Outline white blood cells.
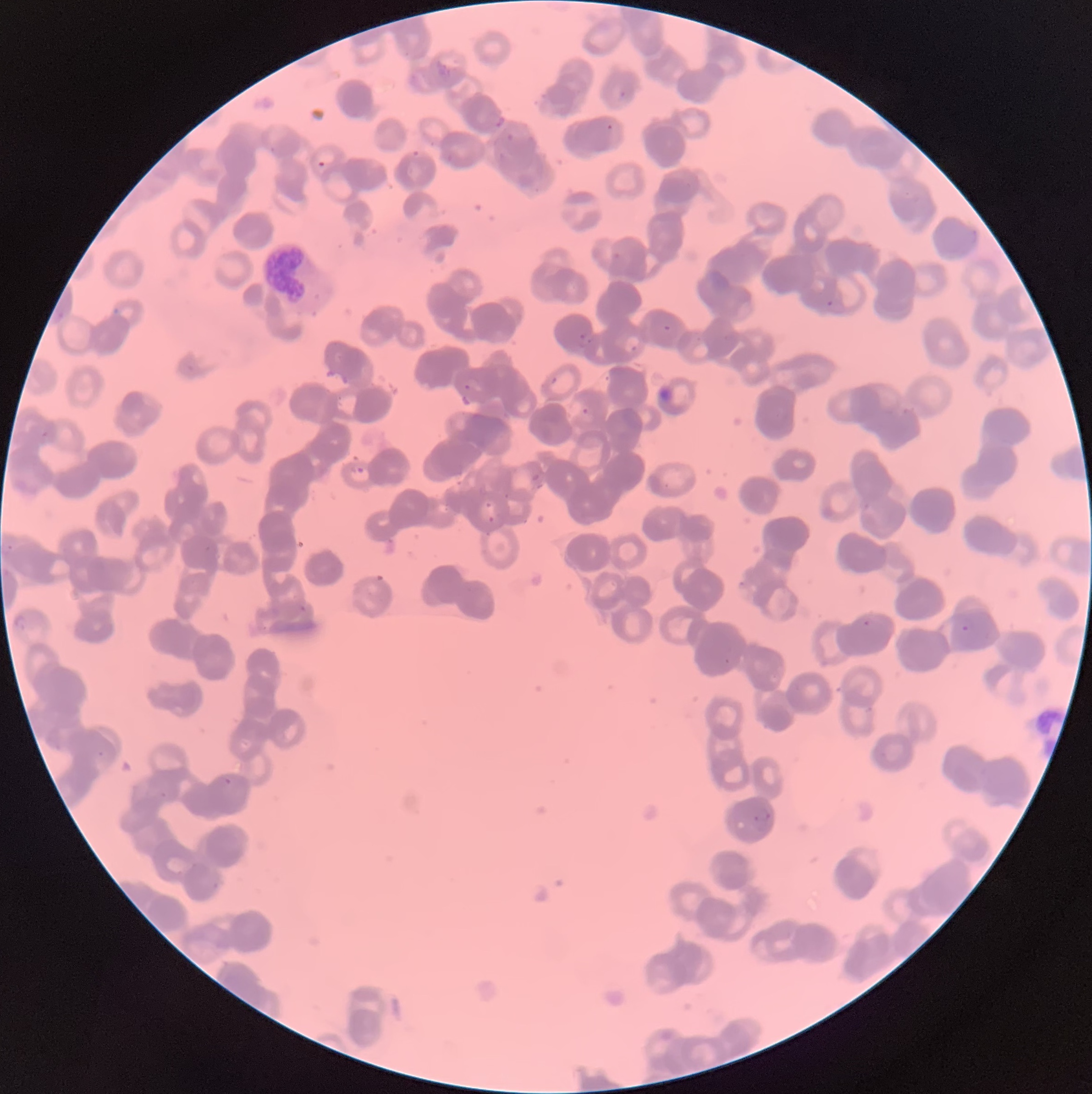
Approximate bounding boxes as [x1, y1, x2, y2] in pixels.
White blood cells: [262, 238, 309, 302].

Summary:
  - Plasmodium parasite locations: [620, 91, 633, 102], [494, 116, 506, 129], [412, 150, 422, 158], [317, 160, 327, 167], [614, 252, 621, 260], [827, 299, 834, 307], [664, 324, 672, 331], [577, 332, 592, 348], [630, 345, 642, 356], [549, 376, 558, 385], [581, 406, 590, 415], [350, 464, 365, 475], [532, 474, 540, 481], [478, 500, 495, 524], [12, 614, 31, 632], [863, 618, 872, 629], [960, 624, 970, 633], [223, 776, 233, 785], [160, 792, 168, 799], [753, 806, 773, 824], [211, 882, 219, 891]
  - Plasmodium parasites too small for a box (approximate centers as [x, y] in pixels): [609, 127], [466, 387], [44, 434], [507, 496], [207, 548], [303, 608], [727, 661], [100, 754]
  - Modality: light microscopy
  - Preparation: thin blood film
  - Red blood cell morphology: rouleaux formation
  - Image size: 1092×1094 pixels